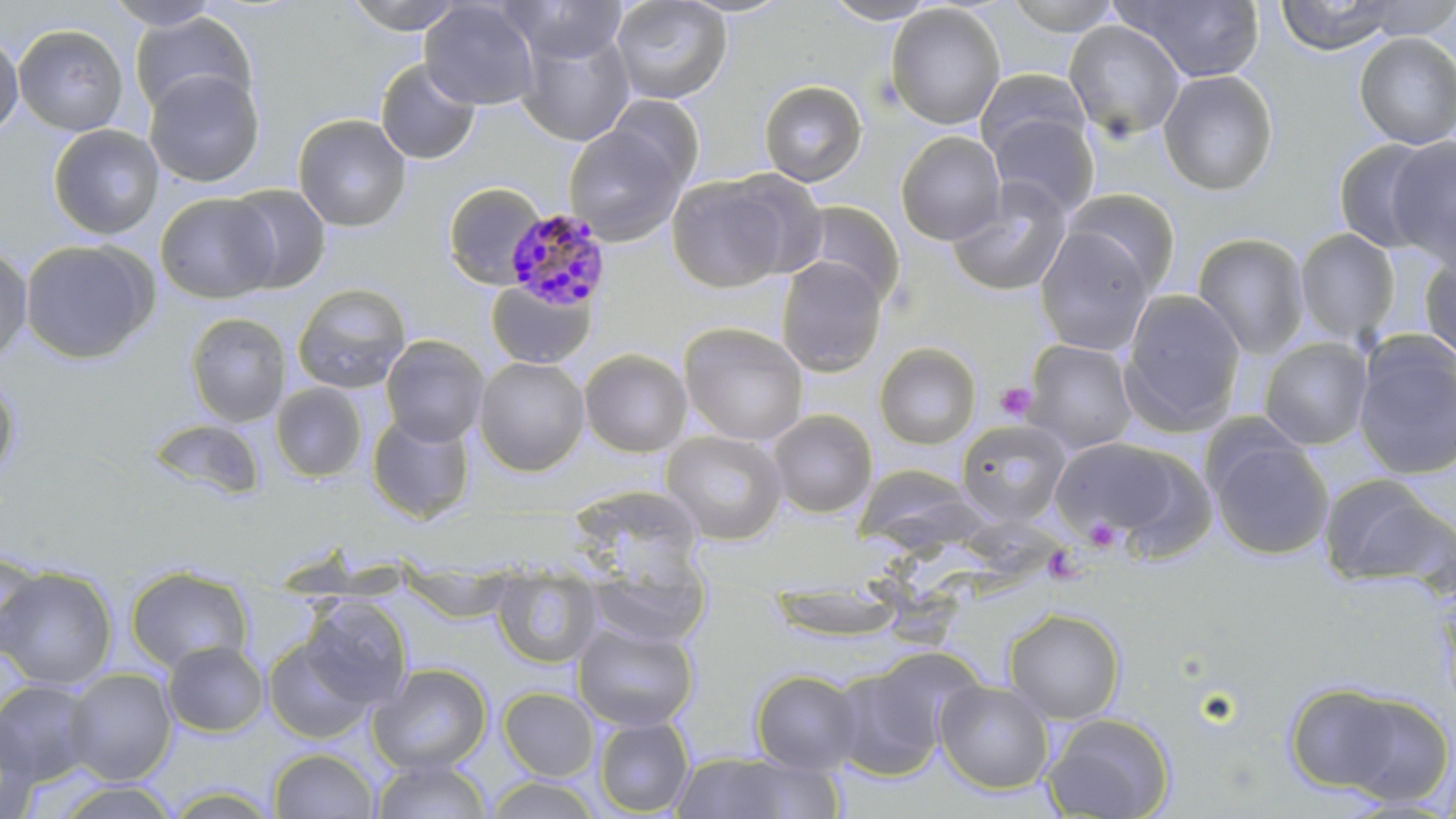

slide-level diagnosis = Plasmodium malariae
field of view = one of a larger specimen
preparation = thin blood smear
image size = 1456×819 pixels
magnification = 1000x
uninfected red blood cell locations = approximate bounding boxes as named x1/y1/x2/y2 corners in pixels: (x1=342, y1=0, x2=470, y2=34), (x1=500, y1=0, x2=629, y2=65), (x1=610, y1=0, x2=732, y2=104), (x1=822, y1=0, x2=939, y2=24), (x1=1003, y1=0, x2=1123, y2=36), (x1=1120, y1=0, x2=1266, y2=82), (x1=1274, y1=0, x2=1398, y2=55), (x1=1356, y1=0, x2=1456, y2=41), (x1=102, y1=1, x2=224, y2=30), (x1=419, y1=1, x2=540, y2=109), (x1=885, y1=3, x2=1006, y2=130), (x1=129, y1=11, x2=257, y2=119), (x1=1063, y1=18, x2=1186, y2=141), (x1=13, y1=24, x2=129, y2=136), (x1=515, y1=25, x2=636, y2=146), (x1=0, y1=31, x2=24, y2=140), (x1=1354, y1=32, x2=1456, y2=149), (x1=375, y1=59, x2=481, y2=165), (x1=975, y1=68, x2=1090, y2=163), (x1=144, y1=70, x2=265, y2=188), (x1=1157, y1=70, x2=1278, y2=196), (x1=321, y1=71, x2=449, y2=208), (x1=758, y1=80, x2=867, y2=186), (x1=605, y1=95, x2=706, y2=191), (x1=987, y1=111, x2=1100, y2=218), (x1=293, y1=114, x2=412, y2=232), (x1=47, y1=124, x2=164, y2=240), (x1=563, y1=125, x2=686, y2=245), (x1=895, y1=131, x2=1006, y2=245), (x1=1386, y1=136, x2=1456, y2=268), (x1=1331, y1=137, x2=1445, y2=254), (x1=722, y1=167, x2=829, y2=279), (x1=666, y1=173, x2=792, y2=292), (x1=948, y1=177, x2=1073, y2=297), (x1=443, y1=182, x2=547, y2=289), (x1=223, y1=184, x2=331, y2=293), (x1=1065, y1=188, x2=1180, y2=295), (x1=155, y1=193, x2=279, y2=303), (x1=792, y1=201, x2=906, y2=306), (x1=1035, y1=227, x2=1155, y2=356), (x1=1295, y1=228, x2=1401, y2=343), (x1=1192, y1=233, x2=1310, y2=359), (x1=20, y1=239, x2=157, y2=364), (x1=0, y1=242, x2=33, y2=365), (x1=1419, y1=253, x2=1456, y2=364), (x1=776, y1=255, x2=888, y2=376), (x1=485, y1=279, x2=594, y2=369), (x1=292, y1=283, x2=412, y2=395), (x1=1119, y1=288, x2=1246, y2=435), (x1=185, y1=312, x2=291, y2=428), (x1=679, y1=322, x2=809, y2=446), (x1=1352, y1=332, x2=1455, y2=481), (x1=380, y1=334, x2=489, y2=446), (x1=1258, y1=337, x2=1373, y2=450), (x1=1023, y1=340, x2=1138, y2=454), (x1=874, y1=342, x2=982, y2=449), (x1=579, y1=348, x2=693, y2=457), (x1=474, y1=355, x2=590, y2=476), (x1=0, y1=372, x2=20, y2=483), (x1=270, y1=383, x2=368, y2=482), (x1=767, y1=409, x2=877, y2=519), (x1=366, y1=413, x2=475, y2=522), (x1=148, y1=418, x2=265, y2=501), (x1=955, y1=419, x2=1071, y2=526), (x1=1204, y1=428, x2=1334, y2=561), (x1=659, y1=429, x2=788, y2=545), (x1=1052, y1=436, x2=1207, y2=551), (x1=859, y1=464, x2=979, y2=561), (x1=1318, y1=473, x2=1453, y2=590), (x1=580, y1=490, x2=704, y2=581), (x1=0, y1=551, x2=46, y2=657), (x1=400, y1=563, x2=514, y2=623), (x1=490, y1=565, x2=602, y2=669), (x1=125, y1=566, x2=254, y2=674), (x1=583, y1=566, x2=710, y2=648), (x1=0, y1=567, x2=117, y2=690), (x1=300, y1=598, x2=413, y2=708), (x1=1003, y1=608, x2=1125, y2=723), (x1=573, y1=621, x2=699, y2=732), (x1=263, y1=635, x2=376, y2=744), (x1=162, y1=641, x2=269, y2=737), (x1=829, y1=654, x2=957, y2=782), (x1=368, y1=662, x2=492, y2=774), (x1=63, y1=668, x2=177, y2=785), (x1=750, y1=669, x2=865, y2=775), (x1=935, y1=678, x2=1054, y2=794), (x1=1, y1=679, x2=99, y2=786), (x1=1285, y1=682, x2=1445, y2=801), (x1=499, y1=687, x2=599, y2=781), (x1=1042, y1=712, x2=1174, y2=819), (x1=0, y1=713, x2=41, y2=817), (x1=593, y1=716, x2=694, y2=816), (x1=268, y1=748, x2=380, y2=818), (x1=667, y1=751, x2=831, y2=818), (x1=370, y1=757, x2=491, y2=818), (x1=484, y1=776, x2=602, y2=818)
stain = May-Grünwald-Giemsa
platelet locations = approximate bounding boxes as named x1/y1/x2/y2 corners in pixels: (x1=996, y1=381, x2=1037, y2=422), (x1=1084, y1=516, x2=1122, y2=551), (x1=1043, y1=544, x2=1086, y2=585)
Plasmodium malariae-infected red blood cell locations = approximate bounding boxes as named x1/y1/x2/y2 corners in pixels: (x1=503, y1=207, x2=613, y2=311)
modality = optical microscopy